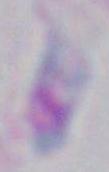
Summary:
  - Identification: Toxoplasma gondii
  - Magnification: 1000x
  - Modality: micrograph